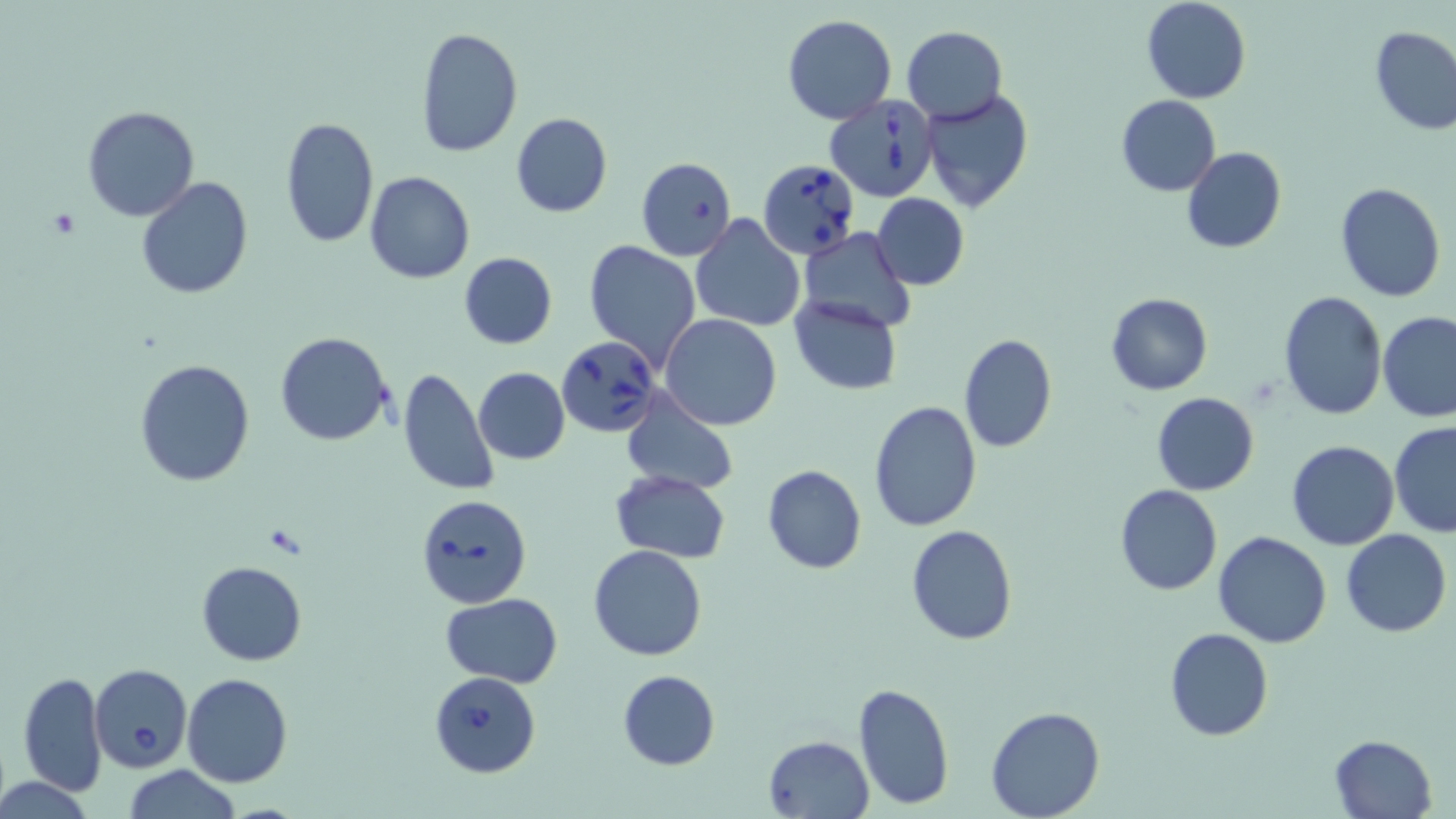 Approximate bounding boxes as [x1, y1, x2, y2] in pixels. Babesia divergens-infected red blood cell locations: [826, 95, 940, 201], [757, 159, 862, 259], [559, 337, 666, 438], [415, 493, 532, 609], [89, 663, 193, 772], [430, 670, 541, 778]. Uninfected red blood cell locations: [1140, 0, 1252, 103], [783, 14, 896, 125], [414, 26, 522, 159], [903, 26, 1006, 122], [1369, 26, 1456, 135], [920, 88, 1035, 213], [1116, 95, 1221, 194], [81, 105, 200, 221], [510, 112, 612, 218], [279, 117, 379, 248], [1181, 146, 1286, 253], [636, 157, 738, 260], [363, 171, 475, 284], [136, 175, 254, 298], [1336, 182, 1445, 301], [870, 193, 970, 291], [690, 214, 807, 332], [798, 226, 915, 334], [584, 239, 702, 371], [459, 252, 557, 348], [1278, 290, 1388, 422], [1104, 292, 1213, 395], [790, 295, 906, 394], [1378, 310, 1456, 422], [660, 314, 782, 430], [275, 333, 393, 445], [958, 334, 1056, 454], [134, 358, 255, 487], [472, 366, 571, 465], [396, 367, 500, 497], [619, 389, 738, 496], [1152, 390, 1259, 495], [867, 400, 984, 533], [1388, 421, 1456, 538], [1286, 440, 1400, 551], [762, 464, 867, 574], [610, 469, 730, 562], [1114, 485, 1222, 595], [905, 525, 1018, 644], [1340, 529, 1452, 637], [1213, 530, 1333, 648], [589, 544, 706, 661], [196, 560, 307, 665], [441, 593, 564, 686], [1164, 627, 1274, 742], [617, 668, 720, 769], [17, 670, 108, 794], [182, 674, 294, 788], [852, 682, 955, 811], [985, 705, 1105, 819], [764, 734, 873, 817], [1330, 734, 1439, 819], [123, 766, 243, 819], [1, 777, 95, 818]. Slide-level diagnosis: Babesia divergens. 1000x magnification. Single field of view. Thin blood film. May-Grünwald-Giemsa-stained preparation. Light microscopy. Image is 1456×819 pixels.